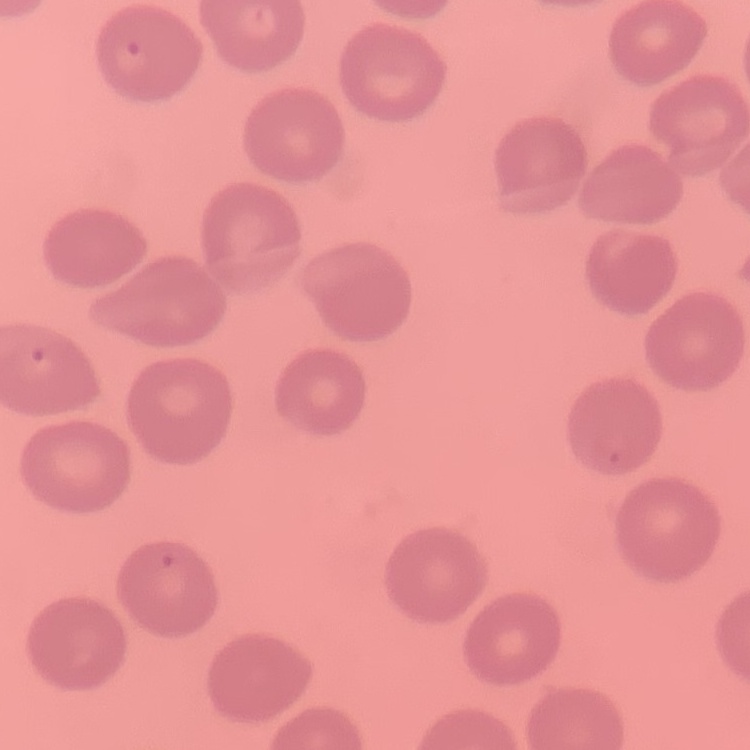

The erythrocytes exhibit no rouleaux formation. Field's or Giemsa stain. One tile cut from a larger photomicrograph. Thin peripheral smear.